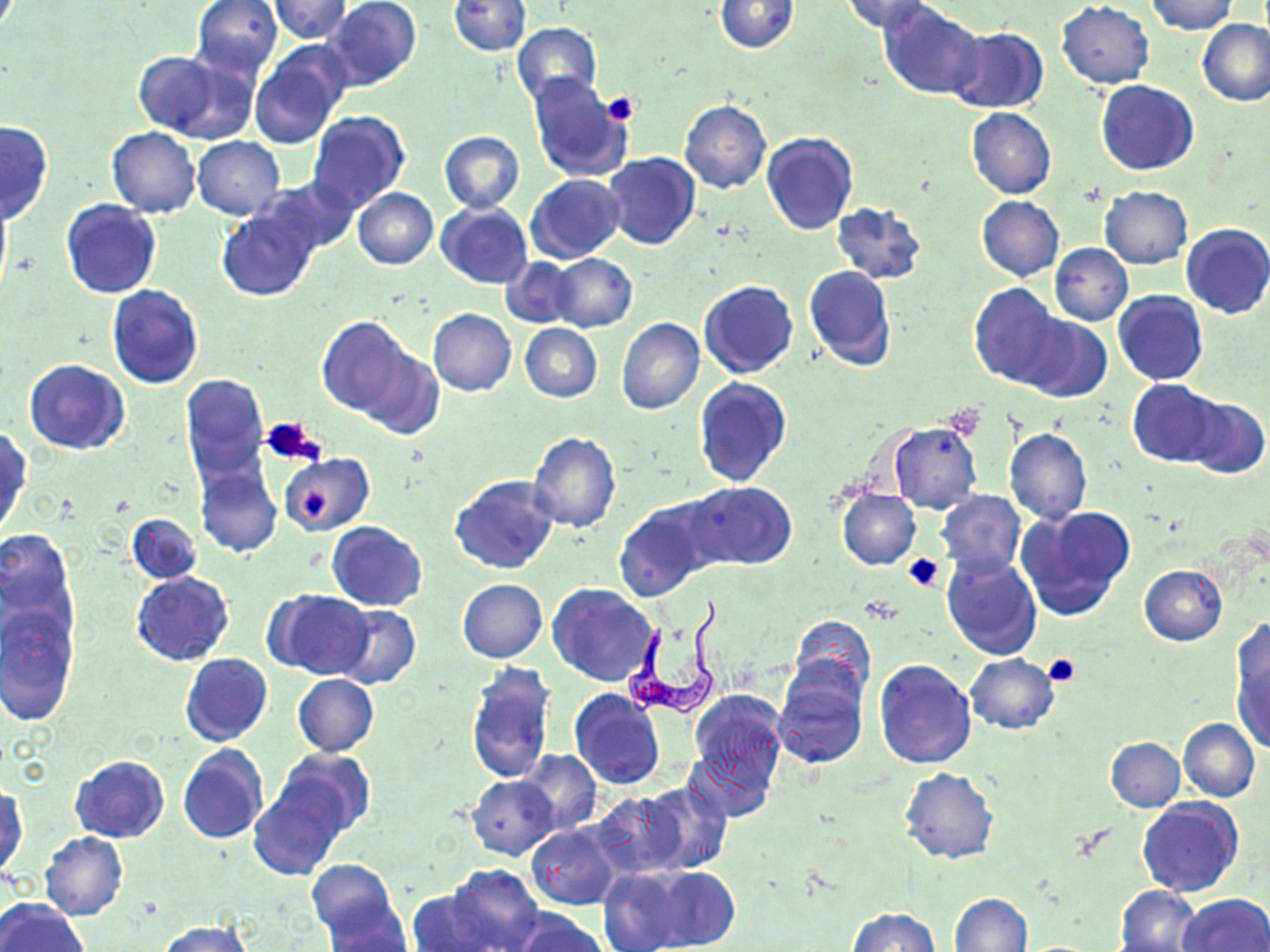
slide_level_diagnosis: Trypanosoma brucei
preparation: thin blood film
modality: optical microscopy
magnification: 1000x
trypanosoma_brucei_locations: 'approximate bounding boxes as (x1, y1, x2, y2) in pixels: (624, 608, 724, 723)'
platelet_locations: 'approximate bounding boxes as (x1, y1, x2, y2) in pixels: (599, 91, 640, 127), (944, 405, 984, 440), (263, 417, 324, 467), (298, 489, 332, 520), (903, 551, 946, 592), (1043, 652, 1081, 688)'
image_size: 1270×952 pixels
uninfected_red_blood_cell_locations: 'approximate bounding boxes as (x1, y1, x2, y2) in pixels: (191, 0, 283, 78), (324, 0, 422, 91), (839, 0, 938, 35), (1145, 0, 1238, 34), (270, 1, 353, 41), (449, 1, 530, 55), (714, 1, 798, 53), (880, 2, 984, 99), (1056, 2, 1154, 88), (1198, 19, 1270, 106), (512, 23, 601, 103), (945, 27, 1048, 114), (250, 42, 351, 147), (131, 51, 226, 137), (169, 59, 267, 197), (526, 73, 630, 182), (1095, 80, 1199, 175), (680, 100, 772, 194), (966, 107, 1056, 200), (306, 111, 411, 214), (0, 120, 53, 225), (108, 127, 200, 218), (439, 130, 524, 212), (761, 132, 858, 236), (192, 137, 285, 219), (603, 153, 702, 250), (526, 175, 624, 262), (257, 178, 359, 256), (1100, 186, 1192, 269), (352, 187, 437, 269), (976, 196, 1064, 281), (60, 199, 162, 299), (830, 200, 926, 285), (436, 203, 533, 287), (216, 204, 320, 302), (1181, 222, 1270, 319), (1049, 244, 1132, 325), (550, 253, 637, 333), (500, 257, 578, 328), (803, 265, 896, 372), (698, 280, 800, 379), (969, 283, 1062, 387), (106, 285, 204, 390), (1112, 290, 1209, 385), (428, 309, 516, 396), (1014, 313, 1112, 402), (317, 316, 414, 418), (617, 319, 704, 416), (520, 323, 602, 402), (359, 344, 444, 441), (23, 360, 130, 454), (179, 373, 270, 486), (692, 378, 792, 487), (1127, 379, 1225, 466), (1184, 397, 1268, 478), (888, 422, 981, 515), (1003, 427, 1093, 523), (0, 428, 32, 539), (527, 430, 622, 533), (279, 453, 373, 537), (195, 463, 282, 558), (448, 475, 560, 576), (686, 481, 796, 570), (836, 488, 920, 570), (935, 489, 1026, 577), (613, 502, 712, 603), (1016, 504, 1138, 621), (126, 512, 201, 584), (326, 521, 427, 611), (0, 531, 78, 658), (941, 551, 1042, 661), (1139, 565, 1227, 644), (131, 571, 233, 666), (458, 579, 546, 662), (548, 583, 659, 686), (269, 589, 374, 679), (0, 601, 79, 728), (334, 604, 419, 690), (788, 615, 875, 705), (1230, 629, 1270, 753), (180, 653, 272, 747), (966, 654, 1060, 733), (873, 659, 976, 768), (465, 661, 557, 785), (771, 665, 868, 768), (292, 674, 378, 755), (569, 690, 664, 789), (687, 691, 787, 795), (1178, 717, 1259, 801), (685, 732, 780, 822), (1105, 737, 1184, 811), (177, 744, 269, 843), (274, 749, 375, 838), (519, 751, 601, 834), (70, 755, 170, 843), (900, 768, 998, 864), (467, 775, 558, 859), (641, 782, 732, 873), (249, 784, 346, 881), (1, 785, 28, 880), (590, 793, 688, 880), (1138, 799, 1243, 897), (526, 825, 621, 910), (39, 832, 128, 922), (306, 859, 403, 945), (442, 865, 545, 952), (645, 866, 739, 950), (599, 868, 689, 951), (1116, 886, 1200, 952), (406, 889, 510, 951), (948, 892, 1032, 952), (1179, 893, 1270, 952), (0, 899, 87, 952), (322, 903, 413, 950), (508, 908, 609, 952), (848, 908, 939, 952), (158, 921, 250, 952)'
stain: May-Grünwald-Giemsa
field_of_view: single